Classify this cell by malaria status.
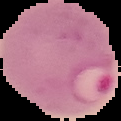
It is parasitized.

preparation = thin blood smear
image type = cell region segmented out of the field of view; surrounding area masked to black
image size = 121×121 pixels